Comment on the morphology of the erythrocytes.
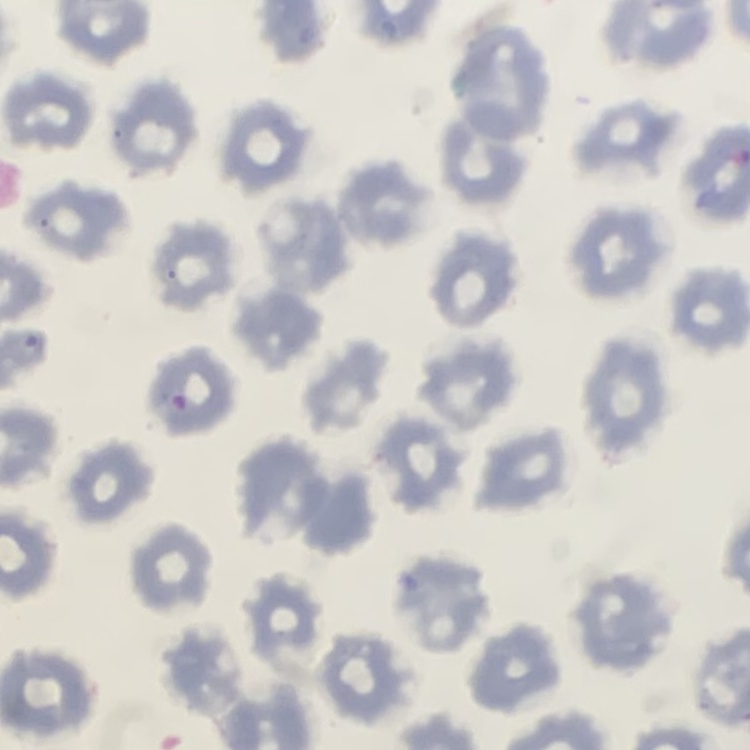
They show no rouleaux formation.

One tile cut from a larger photomicrograph. Thin blood smear. Field's or Giemsa stain.